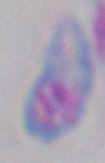
identification: Toxoplasma gondii
modality: micrograph
magnification: 1000x